Locate every malaria parasite.
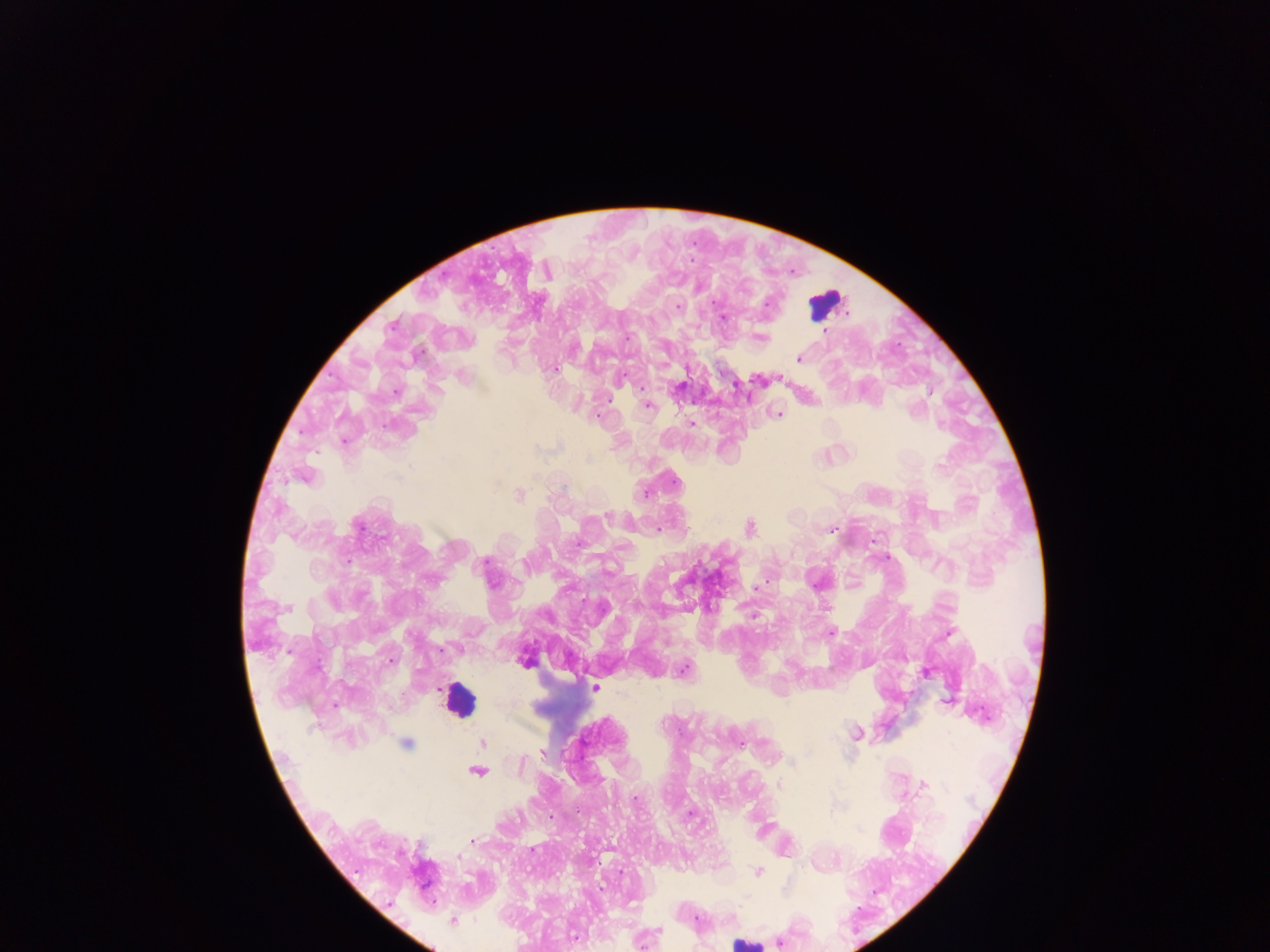
Approximate centers as {x, y} in pixels.
Malaria parasites: {678, 306}, {723, 317}, {825, 332}, {626, 337}, {762, 338}, {798, 359}, {553, 369}, {623, 376}, {396, 393}, {930, 393}, {648, 405}, {914, 410}, {779, 415}, {691, 423}, {941, 425}, {590, 459}, {940, 467}, {304, 477}, {674, 481}, {644, 493}, {519, 495}, {607, 516}, {358, 525}, {750, 528}, {657, 529}, {829, 530}, {578, 542}, {886, 558}, {348, 561}, {484, 563}, {756, 588}, {286, 608}, {752, 617}, {831, 632}, {949, 633}, {442, 649}, {389, 660}, {683, 669}, {926, 673}, {595, 688}, {947, 701}, {856, 734}, {406, 743}, {482, 743}, {741, 744}, {542, 753}, {791, 762}, {477, 771}, {778, 784}, {925, 785}, {635, 799}, {690, 814}, {551, 817}, {472, 841}, {458, 857}, {758, 872}, {602, 888}, {696, 920}, {453, 921}, {659, 930}, {574, 937}, {779, 942}.

{
  "preparation": "thick blood film",
  "image_size": "1270×952 pixels",
  "field_of_view": "single",
  "leukocyte_locations": "approximate centers as {x, y} in pixels: {825, 303}, {458, 699}, {745, 942}",
  "country": "Ghana",
  "capture": "mobile-phone photograph through a microscope"
}